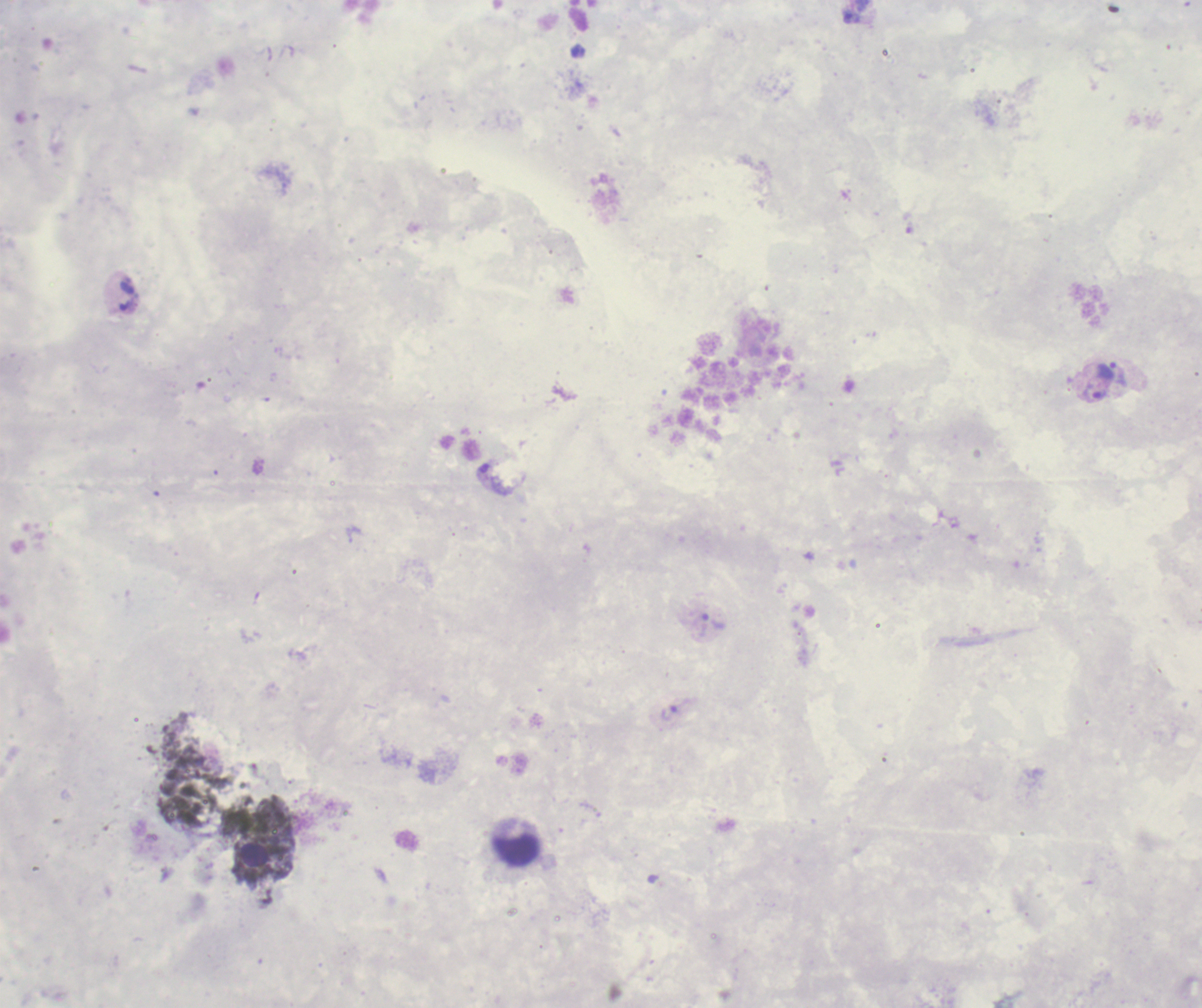
{
  "image_size": "1202×1008 pixels",
  "trophozoite_locations": "approximate centers as {x, y} in pixels: {853, 18}, {128, 295}, {1107, 371}, {1093, 394}, {712, 625}, {670, 713}",
  "field_of_view": "single",
  "magnification": "100x",
  "background_quality": "poor",
  "result": "positive for malaria parasites",
  "stain": "Romanowsky",
  "context": "previously used in an actual diagnosis",
  "leukocyte_locations": "approximate centers as {x, y} in pixels: {516, 849}",
  "preparation": "thick blood film"
}